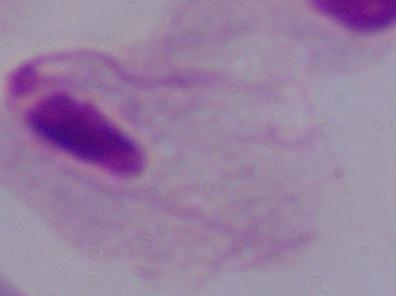

Summary:
  - Magnification: 1000x
  - Identification: trichomonad
  - Modality: micrograph